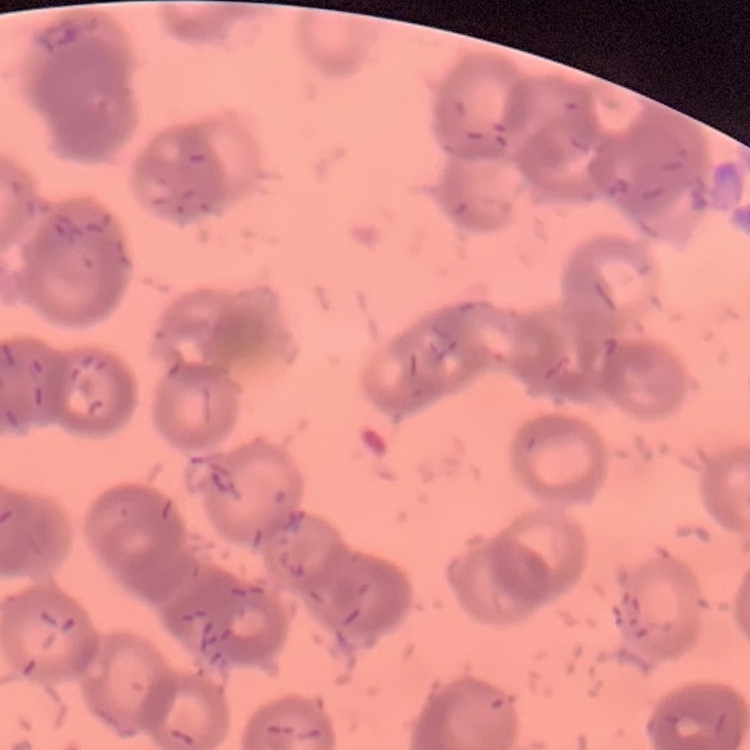
red_blood_cell_morphology: rouleaux formation
stain: Field's or Giemsa
image_type: square crop of a larger photomicrograph
preparation: thin blood smear